Outline each Plasmodium vivax-infected red blood cell.
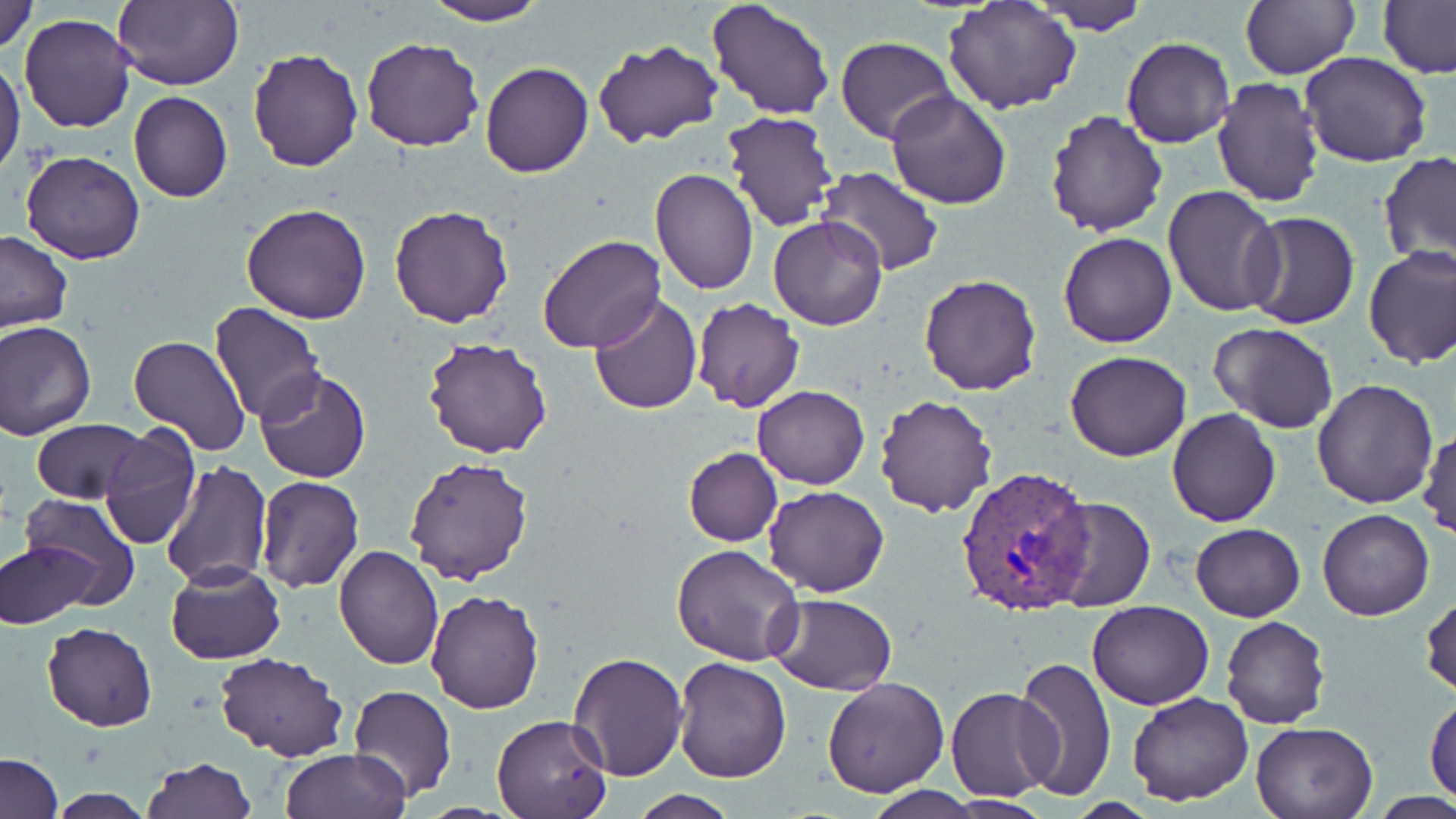

Approximate bounding boxes as named x1/y1/x2/y2 corners in pixels.
Plasmodium vivax-infected red blood cells: (x1=956, y1=467, x2=1096, y2=615).

Uninfected red blood cell locations: (x1=0, y1=0, x2=38, y2=55), (x1=113, y1=0, x2=242, y2=91), (x1=421, y1=0, x2=549, y2=25), (x1=708, y1=0, x2=835, y2=120), (x1=1238, y1=0, x2=1359, y2=81), (x1=1034, y1=1, x2=1149, y2=35), (x1=1378, y1=1, x2=1456, y2=78), (x1=941, y1=2, x2=1082, y2=115), (x1=19, y1=13, x2=138, y2=133), (x1=836, y1=36, x2=957, y2=145), (x1=361, y1=37, x2=484, y2=153), (x1=1121, y1=37, x2=1234, y2=148), (x1=591, y1=38, x2=725, y2=150), (x1=246, y1=47, x2=363, y2=173), (x1=1301, y1=51, x2=1432, y2=168), (x1=0, y1=54, x2=24, y2=181), (x1=481, y1=62, x2=594, y2=178), (x1=1211, y1=76, x2=1326, y2=208), (x1=886, y1=89, x2=1012, y2=210), (x1=128, y1=92, x2=233, y2=203), (x1=722, y1=109, x2=839, y2=232), (x1=1045, y1=109, x2=1169, y2=238), (x1=20, y1=150, x2=145, y2=263), (x1=1378, y1=150, x2=1456, y2=267), (x1=818, y1=166, x2=943, y2=276), (x1=649, y1=169, x2=760, y2=295), (x1=1163, y1=184, x2=1285, y2=318), (x1=241, y1=203, x2=371, y2=323), (x1=389, y1=205, x2=514, y2=329), (x1=1242, y1=211, x2=1360, y2=329), (x1=768, y1=216, x2=888, y2=331), (x1=0, y1=231, x2=72, y2=331), (x1=1059, y1=232, x2=1178, y2=349), (x1=538, y1=235, x2=665, y2=354), (x1=1362, y1=245, x2=1456, y2=369), (x1=917, y1=273, x2=1042, y2=394), (x1=588, y1=292, x2=702, y2=414), (x1=691, y1=296, x2=805, y2=414), (x1=211, y1=302, x2=325, y2=423), (x1=0, y1=321, x2=96, y2=439), (x1=1208, y1=322, x2=1340, y2=434), (x1=129, y1=335, x2=250, y2=458), (x1=423, y1=336, x2=552, y2=460), (x1=1064, y1=351, x2=1193, y2=462), (x1=255, y1=369, x2=371, y2=485), (x1=1311, y1=377, x2=1438, y2=508), (x1=753, y1=385, x2=869, y2=489), (x1=875, y1=394, x2=999, y2=518), (x1=1166, y1=409, x2=1282, y2=528), (x1=30, y1=419, x2=150, y2=504), (x1=98, y1=423, x2=201, y2=551), (x1=1418, y1=426, x2=1455, y2=542), (x1=683, y1=447, x2=782, y2=546), (x1=402, y1=456, x2=533, y2=587), (x1=160, y1=458, x2=270, y2=592), (x1=256, y1=474, x2=365, y2=593), (x1=764, y1=486, x2=889, y2=597), (x1=18, y1=494, x2=142, y2=609), (x1=1045, y1=496, x2=1154, y2=612), (x1=1317, y1=508, x2=1435, y2=621), (x1=1190, y1=523, x2=1305, y2=621), (x1=1, y1=541, x2=97, y2=629), (x1=673, y1=542, x2=803, y2=666), (x1=334, y1=545, x2=444, y2=668), (x1=165, y1=561, x2=286, y2=666), (x1=425, y1=590, x2=543, y2=713), (x1=1421, y1=592, x2=1455, y2=698), (x1=767, y1=593, x2=897, y2=693), (x1=1087, y1=600, x2=1215, y2=710), (x1=1222, y1=616, x2=1331, y2=729), (x1=41, y1=621, x2=159, y2=732), (x1=568, y1=650, x2=687, y2=780), (x1=216, y1=652, x2=345, y2=761), (x1=1014, y1=656, x2=1117, y2=802), (x1=675, y1=657, x2=791, y2=783), (x1=822, y1=677, x2=948, y2=797), (x1=348, y1=684, x2=457, y2=801), (x1=946, y1=687, x2=1061, y2=801), (x1=1127, y1=692, x2=1254, y2=805), (x1=1425, y1=694, x2=1456, y2=802), (x1=491, y1=711, x2=614, y2=819), (x1=1251, y1=719, x2=1379, y2=818), (x1=281, y1=749, x2=408, y2=819), (x1=1, y1=753, x2=61, y2=819), (x1=142, y1=757, x2=256, y2=818), (x1=860, y1=788, x2=985, y2=818), (x1=45, y1=791, x2=157, y2=818), (x1=629, y1=792, x2=741, y2=819), (x1=940, y1=798, x2=1052, y2=817). Slide-level diagnosis: Plasmodium vivax. Image is 1456×819 pixels. Single field of view. May-Grünwald-Giemsa-stained preparation. Light microscopy. Thin blood film. Captured at 1000x magnification.